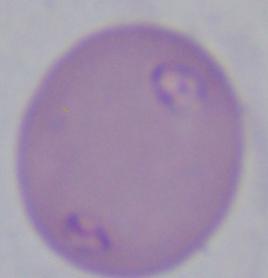

modality: micrograph
magnification: 1000x
identification: Babesia